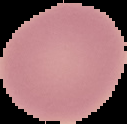
Summary:
  - Preparation: thin blood smear
  - Image size: 127×124 pixels
  - Result: no malaria parasites seen
  - Image type: segmented cell region on a black background